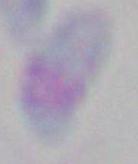
identification = Toxoplasma gondii
modality = photomicrograph
magnification = 1000x